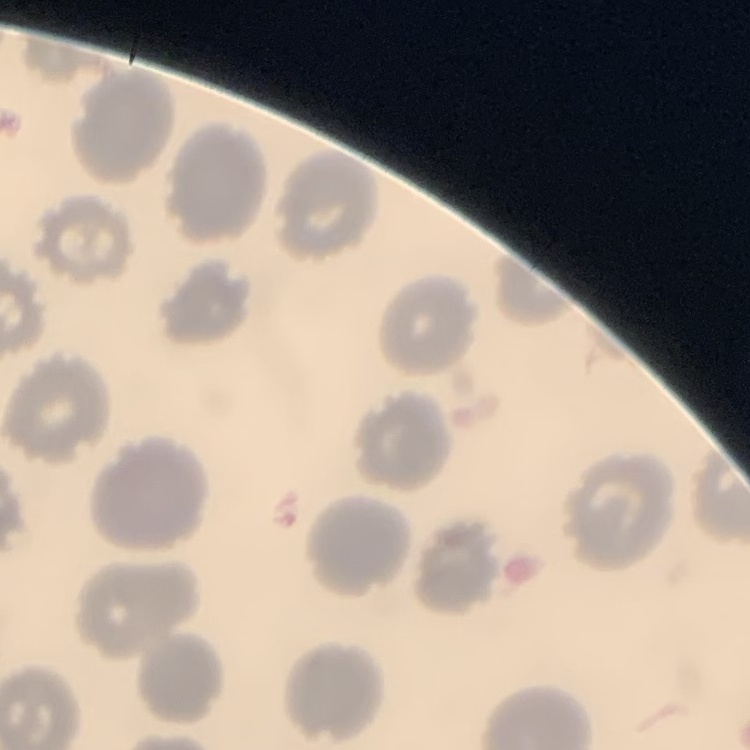
red blood cell morphology = no rouleaux formation
preparation = thin blood film
image type = square crop of a larger photomicrograph
stain = Field's or Giemsa